Classify this cell by malaria status.
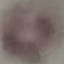
Uninfected.

Giemsa stain. Automatically extracted cell patch, resized to 64 × 64 pixels. Photographed with a smartphone camera at the microscope eyepiece. Thin smear of blood.